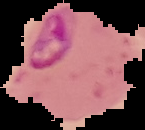

{
  "malaria_status": "parasitized",
  "image_type": "segmented cell region on a black background",
  "image_size": "145×130 pixels",
  "preparation": "thin blood smear"
}